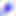

Summary:
  - Modality: micrograph
  - Identification: Toxoplasma gondii
  - Magnification: 400x